Identify the parasite.
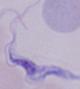

This is a trypanosome.

1000x magnification. Photomicrograph.